Comment on the morphology of the red blood cells.
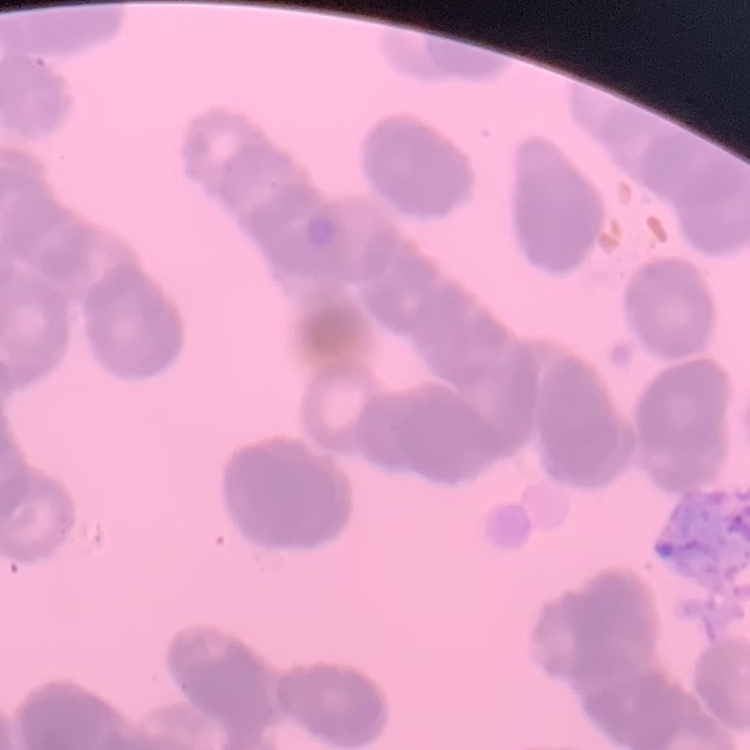
They show rouleaux formation.

Thin peripheral smear. Square crop of a larger photomicrograph. Stained with either Field's or Giemsa.